Classify this cell by malaria status.
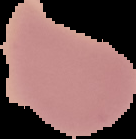
It is uninfected.

Image is 136×139 pixels. From a thin blood smear. The area outside the segmented cell region is set to black.